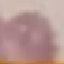

Summary:
  - Result: no malaria parasites detected
  - Capture: smartphone through the microscope eyepiece
  - Image type: cell patch, automatically extracted from a larger field of view and resized to 64 × 64 pixels
  - Stain: Giemsa
  - Preparation: thin blood film